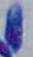
Micrograph. Toxoplasma gondii is seen. Captured at 1000x magnification.